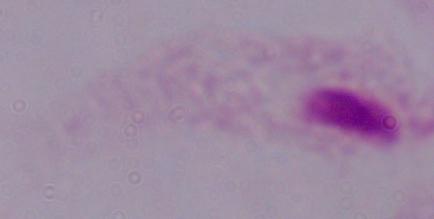
Summary:
  - Magnification: 1000x
  - Identification: trichomonad
  - Modality: photomicrograph